Point out each Plasmodium parasite.
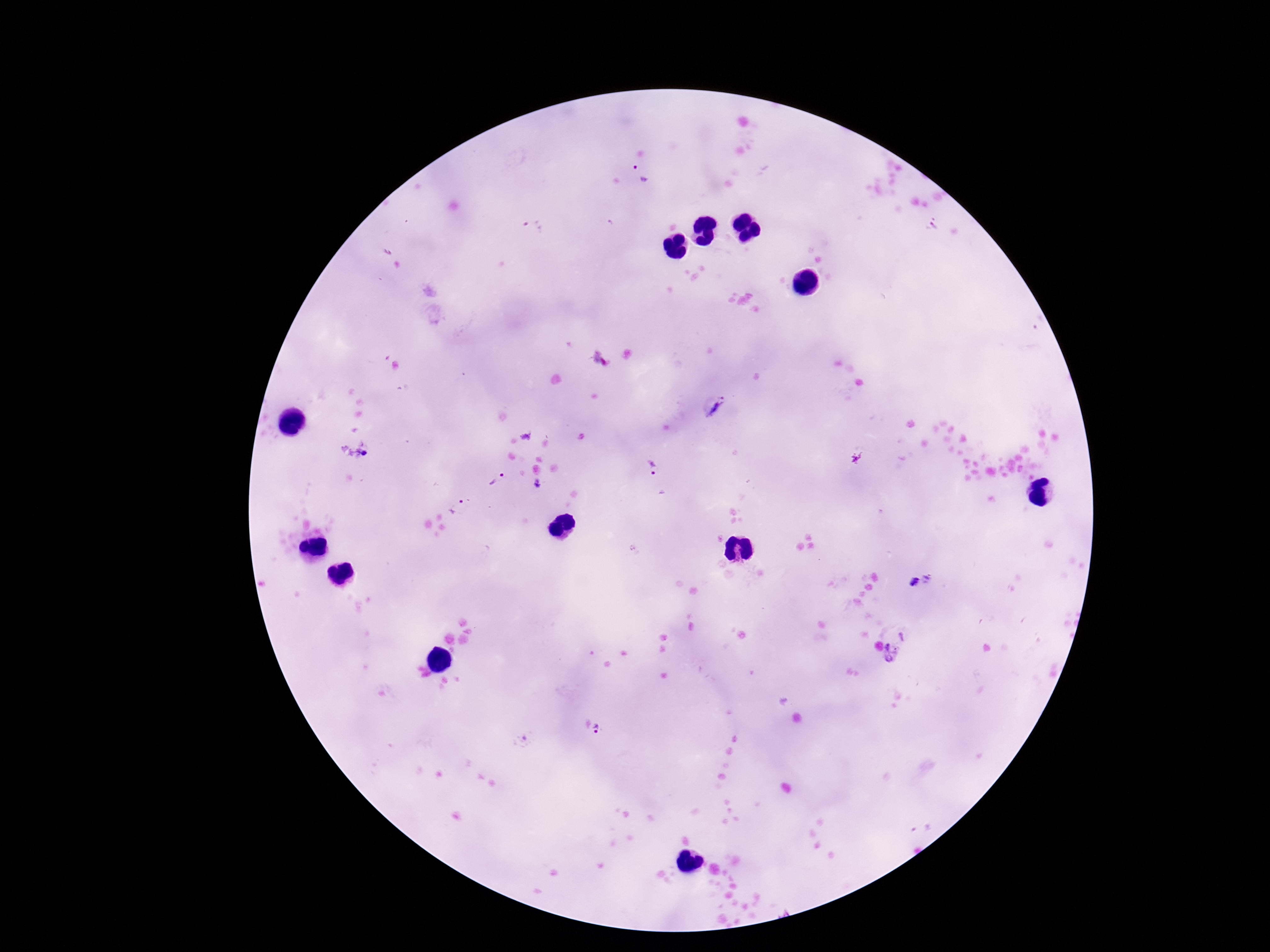
Approximate centers as {x, y} in pixels.
Plasmodium parasites: {643, 175}, {934, 224}, {531, 229}, {715, 408}, {367, 454}, {652, 467}, {495, 478}, {536, 484}, {456, 507}, {929, 578}, {913, 582}, {903, 636}, {892, 653}, {598, 729}.

Summary:
  - Capture: smartphone camera through the microscope eyepiece
  - Stain: Giemsa
  - Magnification: 100x
  - Image size: 1270×952 pixels
  - Patient malaria status: infected
  - Preparation: thick blood film
  - Field of view: one from this slide